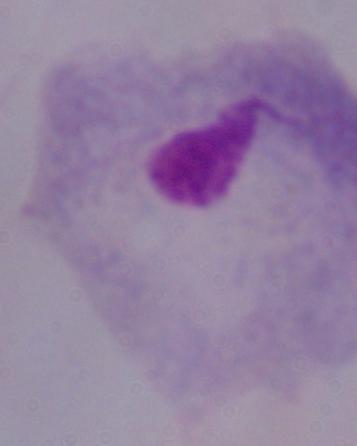

Summary:
  - Identification: trichomonad
  - Modality: micrograph
  - Magnification: 1000x